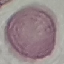

Summary:
  - Result: no malaria parasites detected
  - Preparation: thin blood smear
  - Capture: smartphone through the microscope eyepiece
  - Stain: Giemsa
  - Image type: automatically extracted cell patch, resized to 64 × 64 pixels